Assess the morphology of the red blood cells.
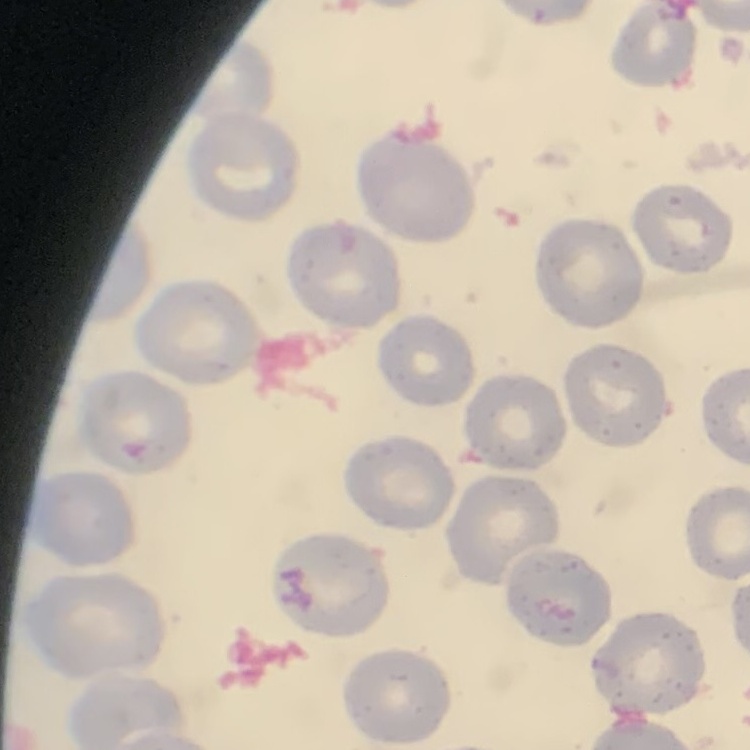
They show no rouleaux formation.

Stained with either Field's or Giemsa. One tile cut from a larger photomicrograph. Thin peripheral smear.